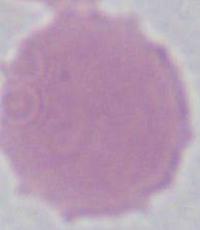
magnification = 1000x
modality = micrograph
identification = erythrocyte